Outline each Plasmodium falciparum-infected red blood cell.
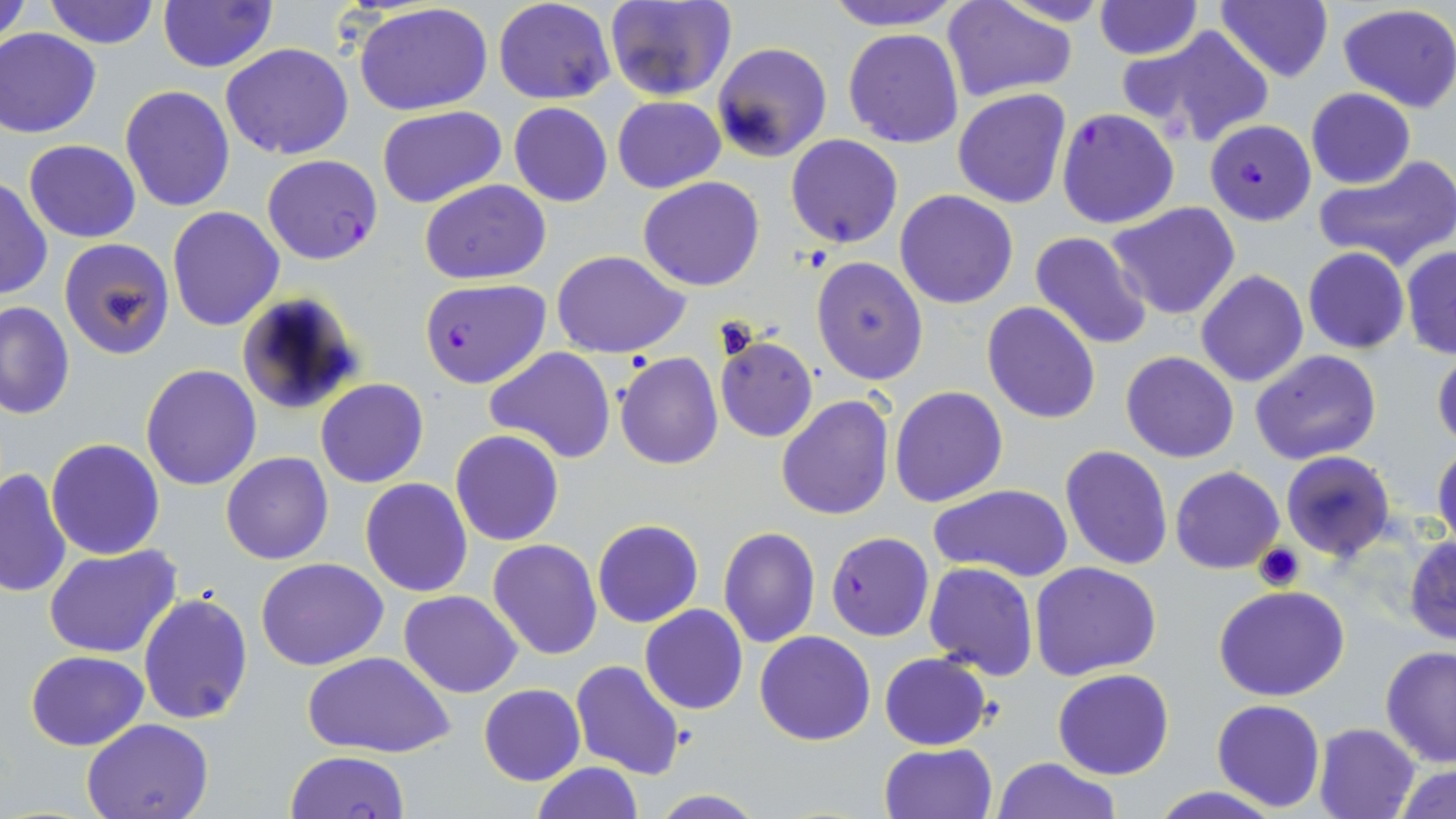
Approximate bounding boxes as [x1, y1, x2, y2] in pixels.
Plasmodium falciparum-infected red blood cells: [1056, 109, 1181, 229], [1204, 120, 1316, 225], [261, 154, 382, 266], [418, 279, 549, 387], [826, 532, 933, 641], [285, 750, 411, 819].

Platelet locations: [1254, 544, 1305, 593]. Uninfected red blood cell locations: [0, 0, 31, 49], [43, 0, 161, 49], [493, 0, 615, 105], [818, 0, 968, 30], [997, 0, 1115, 28], [1215, 0, 1333, 83], [606, 1, 737, 102], [941, 1, 1077, 102], [1094, 1, 1202, 57], [157, 2, 278, 72], [353, 3, 496, 116], [1336, 4, 1456, 113], [1122, 26, 1275, 147], [0, 28, 101, 138], [843, 28, 965, 148], [712, 42, 832, 164], [221, 43, 354, 160], [120, 85, 235, 212], [952, 87, 1072, 209], [1305, 88, 1416, 189], [613, 96, 725, 193], [509, 103, 613, 207], [377, 105, 508, 209], [393, 115, 533, 268], [785, 134, 904, 249], [23, 140, 141, 242], [1315, 153, 1456, 272], [638, 176, 765, 291], [0, 178, 51, 301], [420, 179, 549, 284], [895, 190, 1019, 309], [1107, 200, 1242, 320], [166, 207, 284, 331], [1029, 231, 1153, 351], [58, 238, 175, 359], [1400, 246, 1456, 359], [1303, 247, 1410, 353], [553, 250, 692, 357], [810, 255, 930, 386], [1196, 270, 1308, 388], [232, 291, 366, 415], [0, 300, 75, 419], [982, 300, 1102, 422], [714, 336, 818, 442], [485, 347, 616, 464], [1432, 347, 1456, 451], [1251, 349, 1383, 464], [1120, 351, 1239, 462], [613, 353, 724, 471], [140, 364, 262, 492], [315, 379, 428, 487], [890, 385, 1008, 506], [775, 394, 893, 522], [450, 429, 564, 546], [45, 437, 165, 559], [1433, 442, 1456, 552], [1060, 444, 1173, 570], [1280, 451, 1396, 559], [221, 452, 334, 565], [1171, 466, 1284, 574], [0, 467, 72, 597], [360, 477, 474, 597], [930, 484, 1073, 582], [592, 518, 704, 628], [718, 526, 821, 648], [1404, 535, 1456, 646], [487, 539, 601, 658], [44, 545, 185, 659], [256, 558, 390, 671], [67, 559, 231, 699], [1030, 561, 1163, 681], [922, 562, 1037, 681], [1214, 585, 1350, 700], [138, 590, 253, 724], [398, 590, 522, 697], [640, 605, 748, 714], [756, 631, 875, 746], [1380, 647, 1456, 767], [25, 649, 149, 749], [305, 651, 453, 758], [879, 652, 990, 750], [571, 660, 687, 782], [1053, 669, 1175, 780], [478, 684, 585, 785], [1211, 699, 1325, 812], [82, 717, 215, 819], [1314, 722, 1421, 819], [881, 742, 998, 819], [994, 757, 1121, 819], [531, 761, 642, 818], [1392, 763, 1456, 819], [1147, 787, 1281, 819], [646, 791, 768, 818]. Slide-level diagnosis: Plasmodium falciparum. Light microscopy. 1000x magnification. One field of a larger specimen. Image is 1456×819 pixels. Thin blood film. May-Grünwald-Giemsa-stained preparation.